State which parasite is depicted.
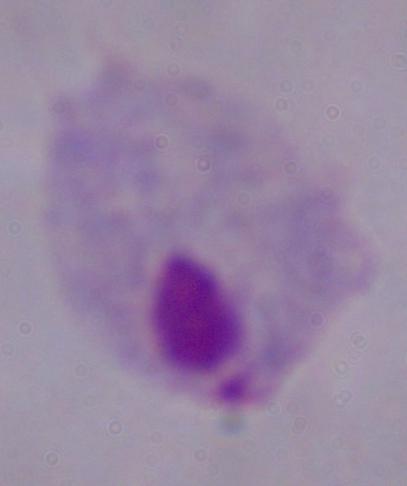
A trichomonad.

Summary:
  - Magnification: 1000x
  - Modality: photomicrograph